Report the malaria status of this cell.
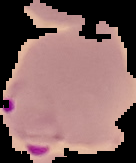
Parasitized.

Summary:
  - Preparation: thin blood smear
  - Image size: 136×163 pixels
  - Image type: segmented cell region with the area outside set to black